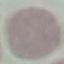
result = negative for malaria parasites
capture = smartphone camera at the microscope eyepiece
stain = Giemsa
image type = automatically extracted cell patch, resized to 64 × 64 pixels
preparation = thin blood film